Describe the morphology of the red blood cells.
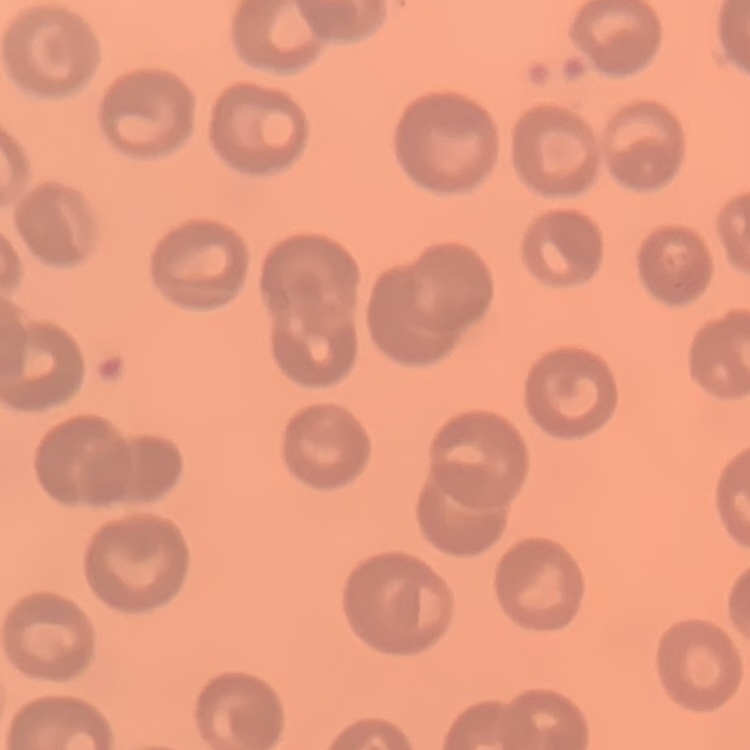

No rouleaux formation.

Summary:
  - Stain: Field's or Giemsa
  - Image type: one tile cut from a larger photomicrograph
  - Preparation: thin blood film